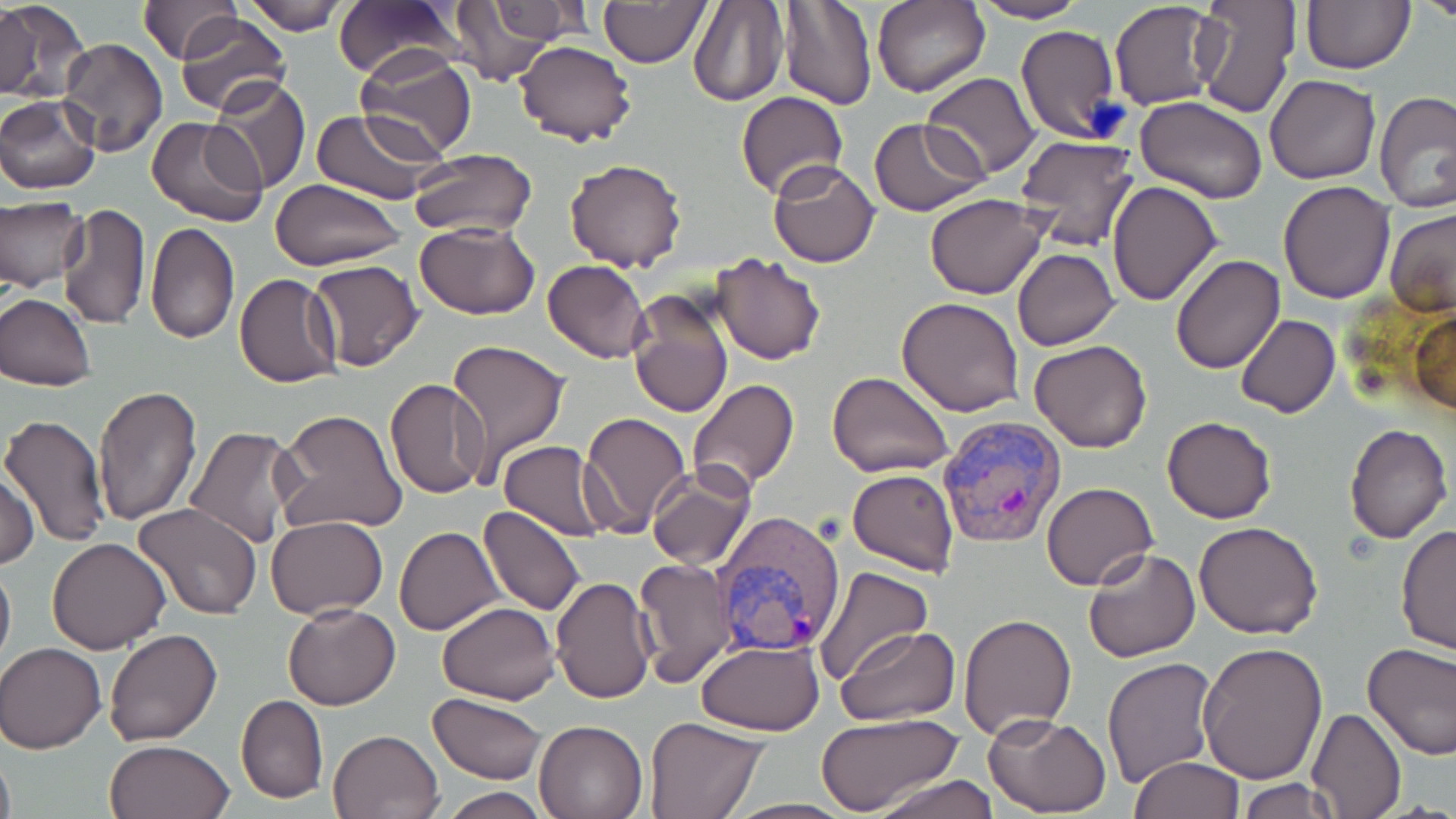
Approximate bounding boxes as [x1, y1, x2, y2] in pixels. Uninfected red blood cell locations: [239, 0, 353, 35], [332, 0, 466, 81], [688, 0, 789, 107], [1301, 0, 1415, 74], [1415, 0, 1456, 24], [446, 1, 564, 88], [598, 1, 709, 67], [776, 1, 876, 109], [873, 1, 990, 97], [972, 1, 1089, 24], [1191, 1, 1300, 119], [0, 2, 89, 104], [136, 2, 241, 65], [1111, 2, 1225, 111], [172, 11, 291, 116], [1015, 25, 1120, 144], [60, 38, 167, 158], [512, 40, 637, 149], [354, 48, 475, 159], [922, 72, 1039, 179], [1265, 74, 1380, 183], [206, 76, 311, 195], [1376, 90, 1456, 211], [736, 91, 848, 200], [0, 94, 102, 194], [1137, 97, 1268, 205], [308, 107, 448, 204], [146, 115, 269, 228], [869, 118, 987, 215], [1014, 135, 1140, 249], [407, 148, 539, 238], [564, 158, 688, 271], [767, 160, 880, 268], [270, 179, 405, 270], [1278, 180, 1396, 303], [1106, 181, 1223, 306], [924, 194, 1048, 299], [0, 198, 88, 293], [59, 205, 149, 331], [1383, 205, 1454, 317], [414, 220, 541, 320], [146, 223, 238, 345], [1012, 247, 1119, 349], [710, 253, 826, 366], [1169, 254, 1286, 374], [307, 258, 424, 374], [543, 260, 651, 364], [234, 275, 343, 388], [626, 291, 733, 421], [0, 292, 97, 391], [897, 297, 1025, 418], [1410, 307, 1454, 416], [1236, 314, 1340, 420], [448, 339, 570, 478], [1029, 339, 1153, 453], [828, 370, 953, 478], [385, 377, 492, 499], [687, 379, 798, 492], [93, 382, 203, 528], [273, 408, 410, 536], [578, 412, 691, 538], [1, 415, 111, 548], [1162, 416, 1277, 523], [1344, 423, 1453, 543], [184, 426, 302, 549], [498, 441, 613, 542], [646, 464, 757, 571], [847, 468, 959, 576], [1, 470, 39, 570], [1041, 482, 1157, 590], [131, 501, 261, 620], [479, 504, 586, 617], [265, 517, 389, 620], [1396, 519, 1455, 657], [1195, 521, 1324, 639], [394, 526, 505, 634], [46, 536, 173, 655], [1085, 536, 1320, 649], [1083, 546, 1201, 664], [0, 551, 15, 678], [633, 558, 736, 687], [813, 565, 932, 685], [550, 575, 658, 704], [436, 601, 558, 704], [283, 602, 400, 711], [957, 611, 1077, 740], [837, 626, 959, 725], [102, 628, 224, 747], [696, 640, 823, 735], [1197, 642, 1328, 785], [1, 643, 106, 753], [1362, 643, 1456, 760], [1101, 658, 1218, 787], [429, 692, 547, 782], [236, 694, 329, 804], [1306, 705, 1406, 819], [815, 713, 963, 817], [983, 713, 1111, 816], [645, 716, 768, 818], [533, 718, 650, 819], [328, 728, 443, 818], [105, 739, 236, 819], [0, 745, 15, 819], [1130, 757, 1242, 818], [872, 773, 1000, 819], [1235, 777, 1346, 817], [439, 787, 548, 819]. Plasmodium vivax-infected red blood cell locations: [937, 414, 1065, 548], [713, 512, 852, 657]. Slide-level diagnosis: Plasmodium vivax. Thin blood film. May-Grünwald-Giemsa stain. Captured at 1000x magnification. Image is 1456×819 pixels. Optical microscopy. One field of a larger specimen.